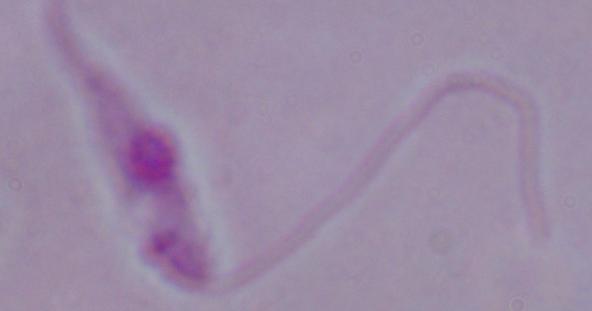
Summary:
  - Magnification: 1000x
  - Modality: photomicrograph
  - Identification: Leishmania